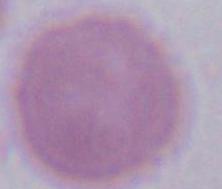

Summary:
  - Modality: micrograph
  - Identification: red blood cell
  - Magnification: 1000x